Comment on the morphology of the red blood cells.
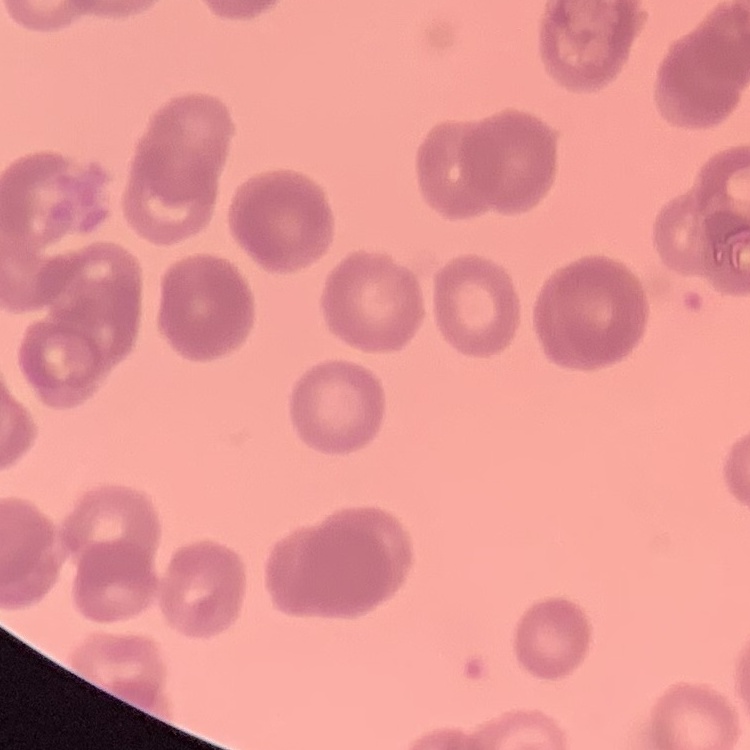

They show rouleaux formation.

Summary:
  - Stain: Field's or Giemsa
  - Preparation: thin blood film
  - Image type: one tile cut from a larger photomicrograph